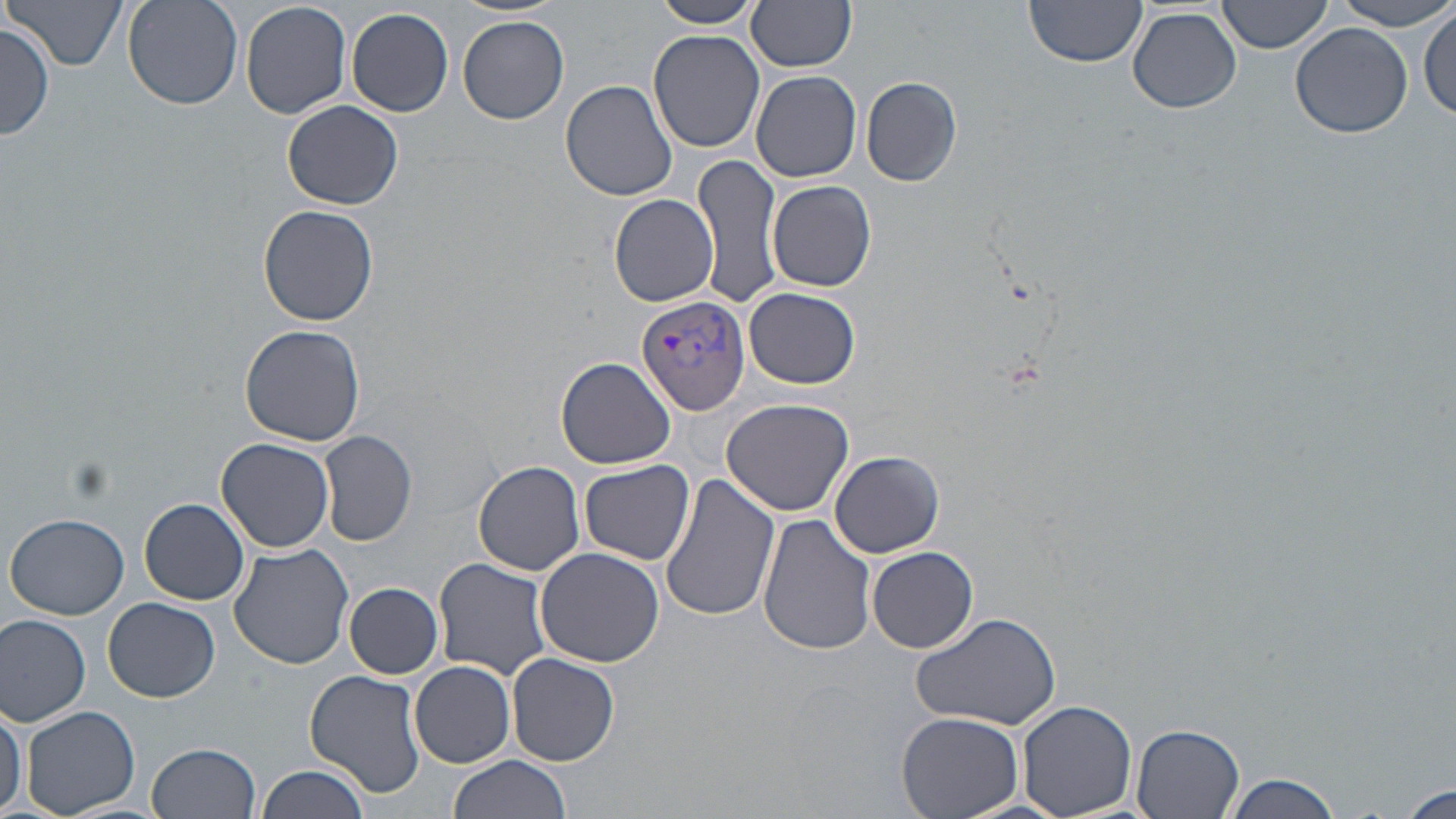

slide-level diagnosis = Plasmodium vivax
uninfected red blood cell locations = approximate bounding boxes as (x1, y1, x2, y2) in pixels: (8, 0, 128, 72), (122, 0, 241, 111), (239, 0, 351, 119), (651, 0, 760, 29), (746, 0, 858, 72), (1025, 0, 1149, 69), (1218, 0, 1333, 55), (1332, 1, 1456, 31), (1129, 5, 1241, 114), (347, 7, 454, 117), (1417, 7, 1455, 120), (458, 16, 570, 124), (0, 22, 54, 140), (1290, 23, 1411, 138), (647, 28, 765, 153), (751, 71, 861, 183), (861, 74, 963, 186), (561, 80, 677, 202), (283, 100, 404, 209), (696, 154, 783, 312), (768, 179, 878, 291), (609, 194, 719, 308), (259, 204, 380, 327), (744, 288, 860, 389), (238, 324, 366, 444), (556, 356, 677, 470), (721, 398, 855, 516), (318, 431, 418, 546), (217, 437, 335, 552), (831, 451, 944, 558), (580, 459, 695, 565), (474, 461, 586, 575), (143, 469, 308, 590), (658, 470, 781, 623), (139, 498, 250, 605), (7, 513, 129, 620), (757, 515, 877, 656), (228, 542, 354, 669), (534, 546, 664, 668), (865, 547, 978, 652), (435, 558, 555, 679), (344, 583, 443, 678), (104, 597, 220, 702), (910, 611, 1064, 730), (0, 615, 92, 727), (507, 652, 622, 766), (409, 660, 516, 769), (305, 669, 426, 796), (1017, 700, 1139, 819), (0, 701, 25, 819), (22, 705, 140, 818), (895, 713, 1024, 819), (1132, 723, 1247, 819), (149, 742, 262, 819), (446, 756, 573, 819), (257, 764, 370, 819), (1221, 772, 1343, 818), (1394, 786, 1454, 819)
stain = May-Grünwald-Giemsa
Plasmodium vivax-infected red blood cell locations = approximate bounding boxes as (x1, y1, x2, y2) in pixels: (634, 294, 751, 417)
modality = optical microscopy
image size = 1456×819 pixels
field of view = single
magnification = 1000x
preparation = thin blood film